Assess this cell for malaria.
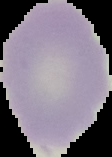
Uninfected.

Image is 112×157 pixels. From a thin blood smear. The area outside the segmented cell region is set to black.